Describe the morphology of the red blood cells.
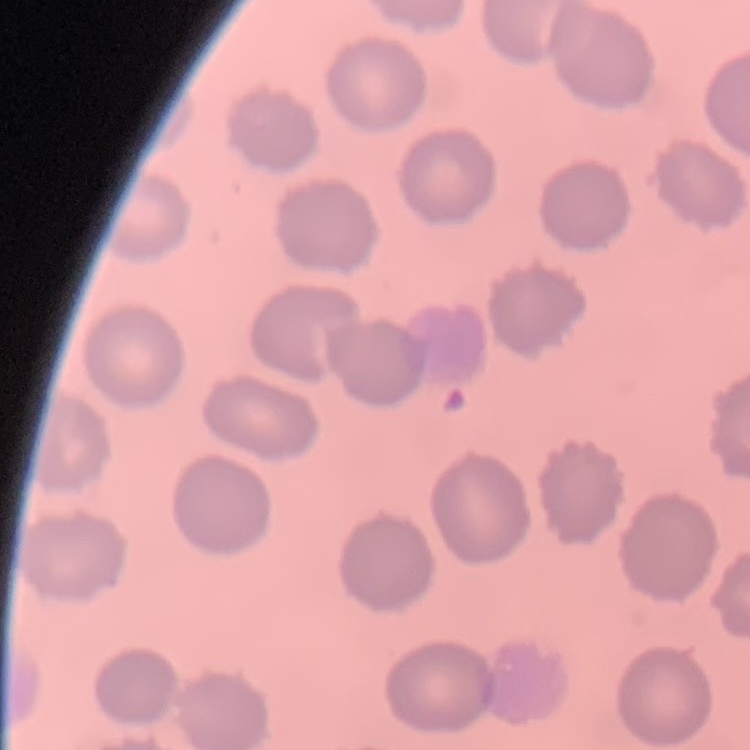

No rouleaux formation.

image type = square crop of a larger photomicrograph
preparation = thin blood smear
stain = Field's or Giemsa